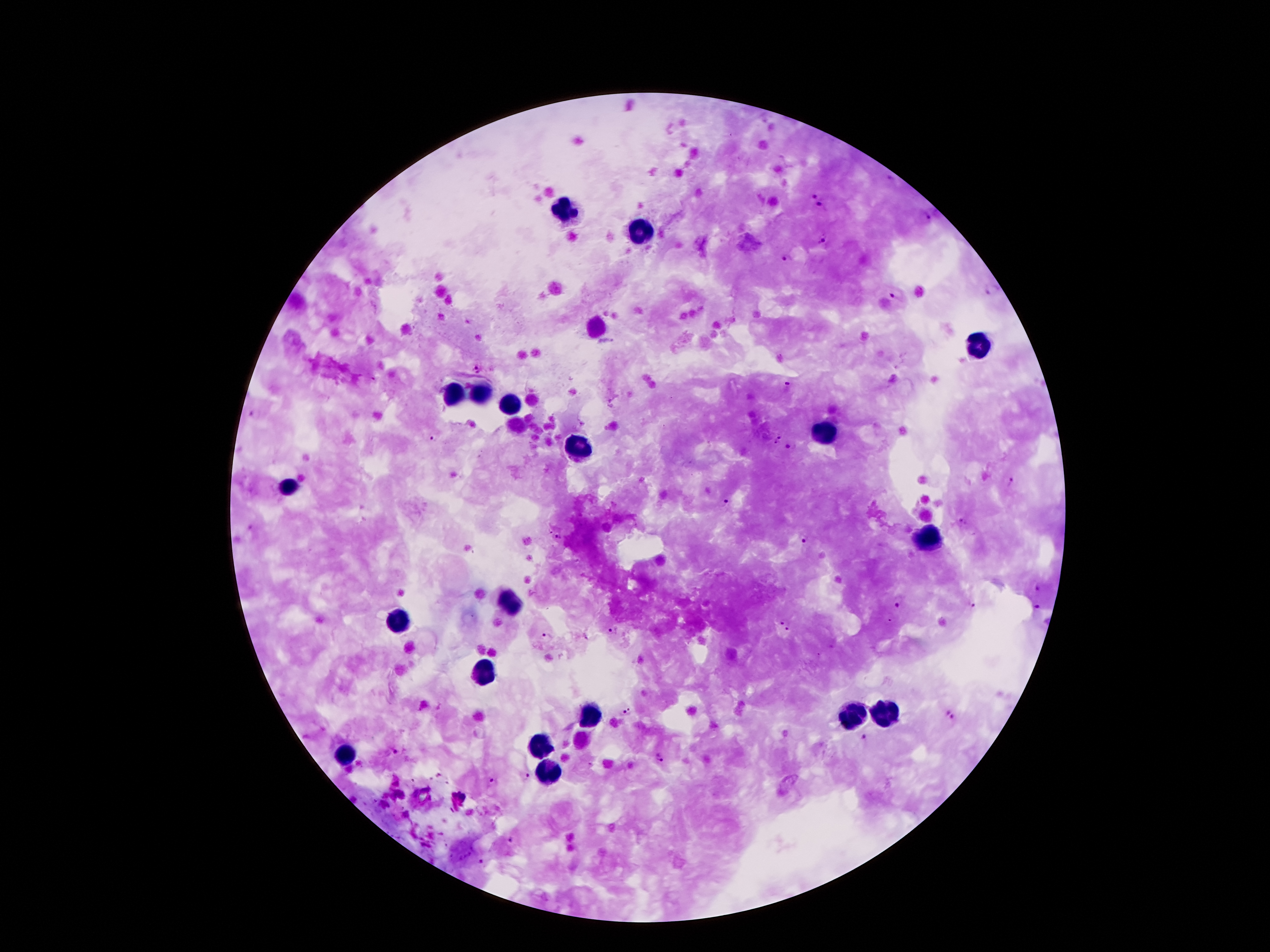 Approximate centers as {x, y} in pixels. Leukocyte locations: {569, 209}, {642, 235}, {978, 342}, {458, 394}, {482, 396}, {515, 406}, {827, 435}, {575, 447}, {288, 487}, {931, 537}, {506, 605}, {397, 619}, {484, 678}, {883, 712}, {588, 716}, {847, 716}, {536, 746}, {343, 755}, {545, 775}. Plasmodium parasite locations: {815, 193}, {822, 207}, {924, 218}, {821, 239}, {784, 257}, {992, 289}, {897, 292}, {478, 366}, {373, 379}, {787, 385}, {254, 415}, {780, 436}, {434, 439}, {774, 444}, {791, 447}, {1012, 483}, {726, 503}, {962, 521}, {550, 530}, {560, 537}, {803, 537}, {1036, 587}, {899, 606}, {973, 607}, {1036, 609}, {785, 624}, {611, 630}, {546, 637}, {626, 711}, {951, 716}, {866, 738}, {394, 752}, {661, 757}, {590, 765}, {526, 777}, {493, 781}, {446, 783}, {512, 840}, {482, 863}. Thick blood film. Patient malaria status: infected with Plasmodium falciparum. Image is 1270×952 pixels. Smartphone photograph taken through the microscope eyepiece. Single field of view. Giemsa stain. 100x magnification.